Report the malaria status of this cell.
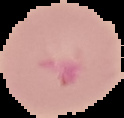
It is parasitized.

preparation = thin blood film
image size = 124×118 pixels
image type = segmented cell region on a black background